State the blood parasite species.
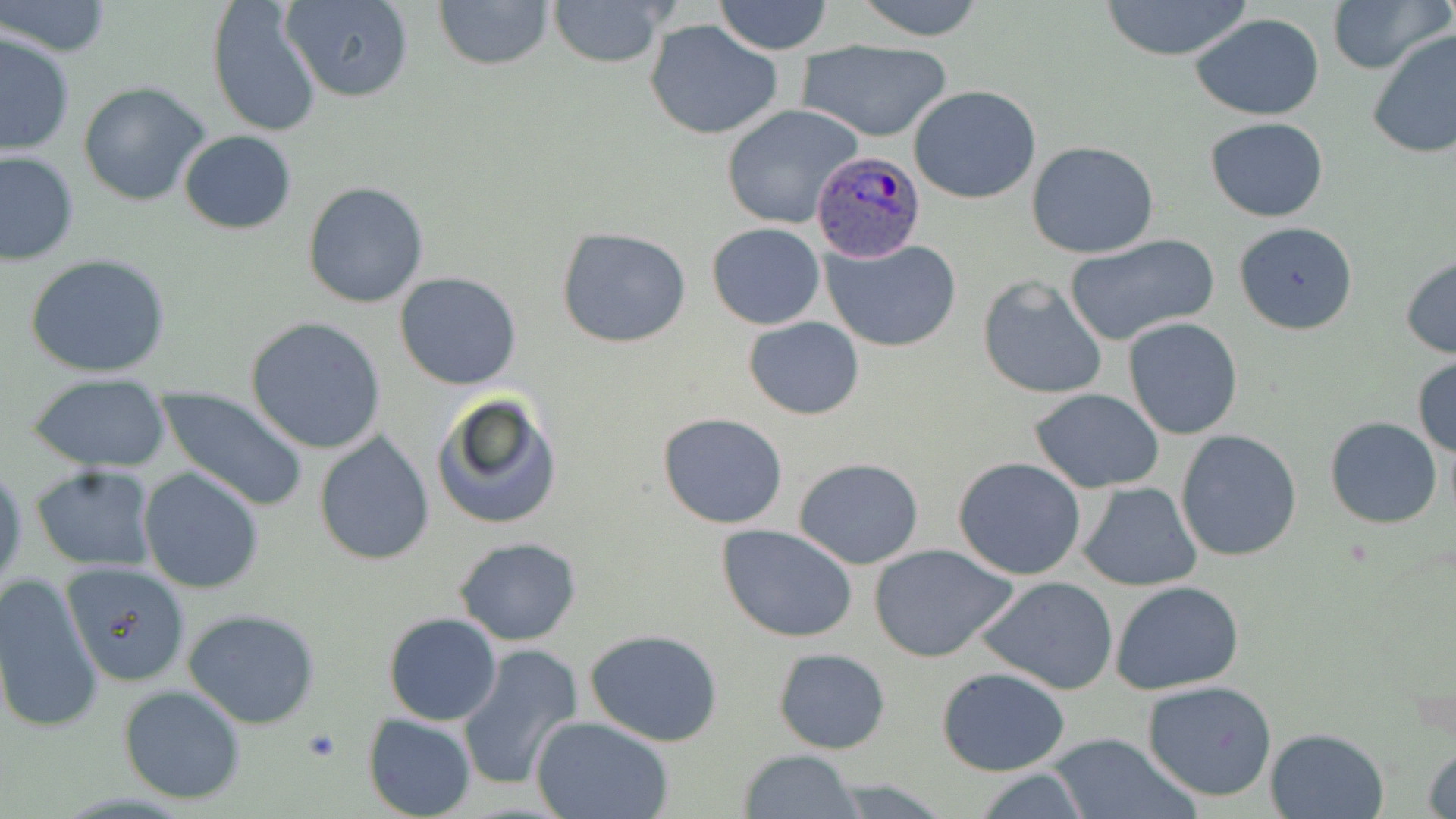
Plasmodium ovale.

Summary:
  - Coordinate format: approximate bounding boxes as named x1/y1/x2/y2 corners in pixels
  - Plasmodium ovale-infected red blood cell locations: (x1=810, y1=149, x2=926, y2=264)
  - Platelet locations: (x1=302, y1=727, x2=342, y2=761)
  - Uninfected red blood cell locations: (x1=282, y1=0, x2=413, y2=103), (x1=433, y1=0, x2=555, y2=70), (x1=547, y1=0, x2=672, y2=69), (x1=714, y1=0, x2=833, y2=55), (x1=852, y1=0, x2=986, y2=42), (x1=1099, y1=0, x2=1253, y2=62), (x1=1325, y1=0, x2=1449, y2=76), (x1=1, y1=1, x2=114, y2=57), (x1=207, y1=1, x2=321, y2=137), (x1=1191, y1=13, x2=1325, y2=120), (x1=644, y1=20, x2=784, y2=141), (x1=1367, y1=29, x2=1456, y2=159), (x1=1, y1=31, x2=75, y2=157), (x1=797, y1=38, x2=953, y2=142), (x1=78, y1=81, x2=213, y2=208), (x1=908, y1=84, x2=1042, y2=204), (x1=721, y1=104, x2=863, y2=231), (x1=1206, y1=118, x2=1330, y2=221), (x1=178, y1=130, x2=297, y2=234), (x1=1026, y1=141, x2=1160, y2=259), (x1=1, y1=150, x2=78, y2=267), (x1=301, y1=180, x2=430, y2=308), (x1=1233, y1=220, x2=1358, y2=335), (x1=706, y1=223, x2=826, y2=330), (x1=557, y1=228, x2=692, y2=348), (x1=1066, y1=235, x2=1219, y2=349), (x1=821, y1=237, x2=963, y2=353), (x1=25, y1=252, x2=170, y2=379), (x1=1400, y1=255, x2=1456, y2=358), (x1=395, y1=272, x2=523, y2=390), (x1=977, y1=274, x2=1109, y2=400), (x1=1123, y1=315, x2=1243, y2=439), (x1=744, y1=316, x2=864, y2=420), (x1=245, y1=317, x2=387, y2=454), (x1=1412, y1=355, x2=1456, y2=458), (x1=28, y1=373, x2=174, y2=472), (x1=155, y1=385, x2=310, y2=512), (x1=1029, y1=387, x2=1164, y2=492), (x1=432, y1=391, x2=562, y2=532), (x1=656, y1=412, x2=789, y2=530), (x1=1325, y1=417, x2=1442, y2=529), (x1=1175, y1=429, x2=1303, y2=561), (x1=314, y1=432, x2=436, y2=564), (x1=952, y1=455, x2=1087, y2=580), (x1=793, y1=458, x2=924, y2=569), (x1=29, y1=464, x2=159, y2=572), (x1=0, y1=467, x2=26, y2=594), (x1=138, y1=467, x2=267, y2=594), (x1=1077, y1=482, x2=1202, y2=590), (x1=717, y1=526, x2=860, y2=643), (x1=453, y1=536, x2=584, y2=645), (x1=869, y1=544, x2=1019, y2=664), (x1=50, y1=559, x2=192, y2=691), (x1=0, y1=572, x2=103, y2=739), (x1=976, y1=575, x2=1119, y2=694), (x1=1111, y1=581, x2=1243, y2=695), (x1=182, y1=608, x2=323, y2=730), (x1=383, y1=613, x2=502, y2=726), (x1=585, y1=629, x2=725, y2=746), (x1=457, y1=642, x2=584, y2=792), (x1=772, y1=647, x2=891, y2=753), (x1=936, y1=666, x2=1070, y2=776), (x1=1142, y1=679, x2=1278, y2=802), (x1=118, y1=685, x2=246, y2=804), (x1=362, y1=713, x2=478, y2=819), (x1=533, y1=717, x2=674, y2=819), (x1=1264, y1=727, x2=1388, y2=818), (x1=1044, y1=732, x2=1192, y2=818), (x1=1423, y1=741, x2=1456, y2=819), (x1=736, y1=749, x2=861, y2=819), (x1=970, y1=767, x2=1094, y2=818), (x1=818, y1=779, x2=962, y2=817)
  - Modality: optical microscopy
  - Stain: May-Grünwald-Giemsa
  - Magnification: 1000x
  - Field of view: single
  - Preparation: thin blood smear
  - Image size: 1456×819 pixels